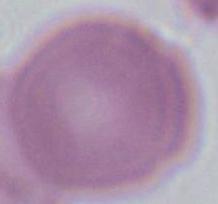
A red blood cell is shown. Micrograph. 1000x magnification.